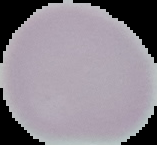
Summary:
  - Image type: segmented cell region on a black background
  - Malaria status: uninfected
  - Image size: 157×145 pixels
  - Preparation: thin blood film